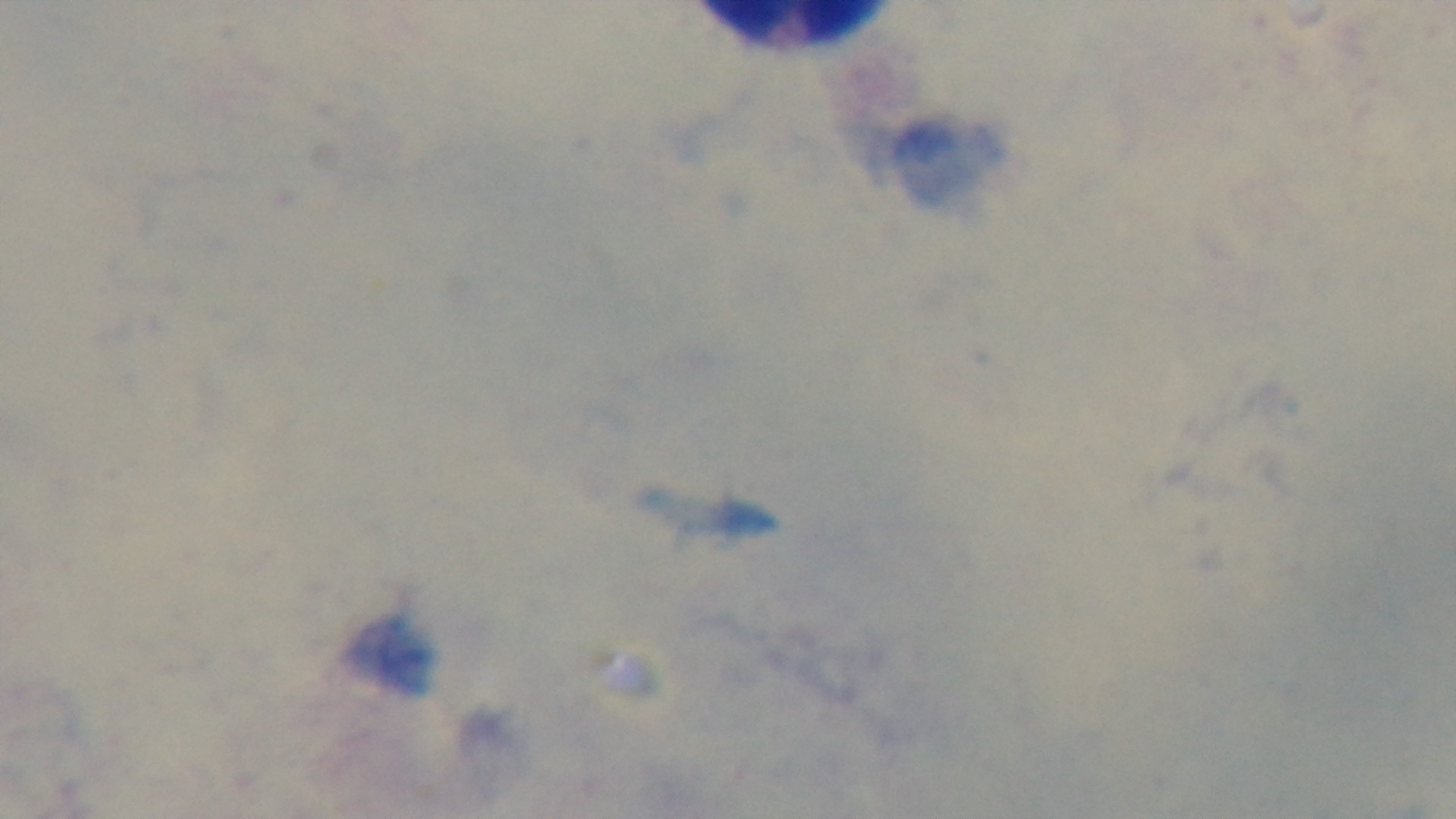

stain = Giemsa
modality = light microscopy
field of view = one from the slide
preparation = thick blood film
capture = mounted 4K digital camera
objective = 100x oil immersion
malaria status = negative